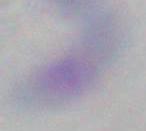
{
  "identification": "Toxoplasma gondii",
  "magnification": "1000x",
  "modality": "photomicrograph"
}